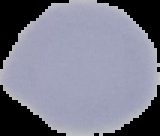 Image is 160×136 pixels. The area outside the segmented cell region is set to black. From a thin blood smear. Malaria status: uninfected.